Classify this cell by malaria status.
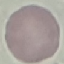
Uninfected.

Summary:
  - Preparation: thin blood smear
  - Capture: smartphone through the microscope eyepiece
  - Image type: automatically extracted cell patch, resized to 64 × 64 pixels
  - Stain: Giemsa